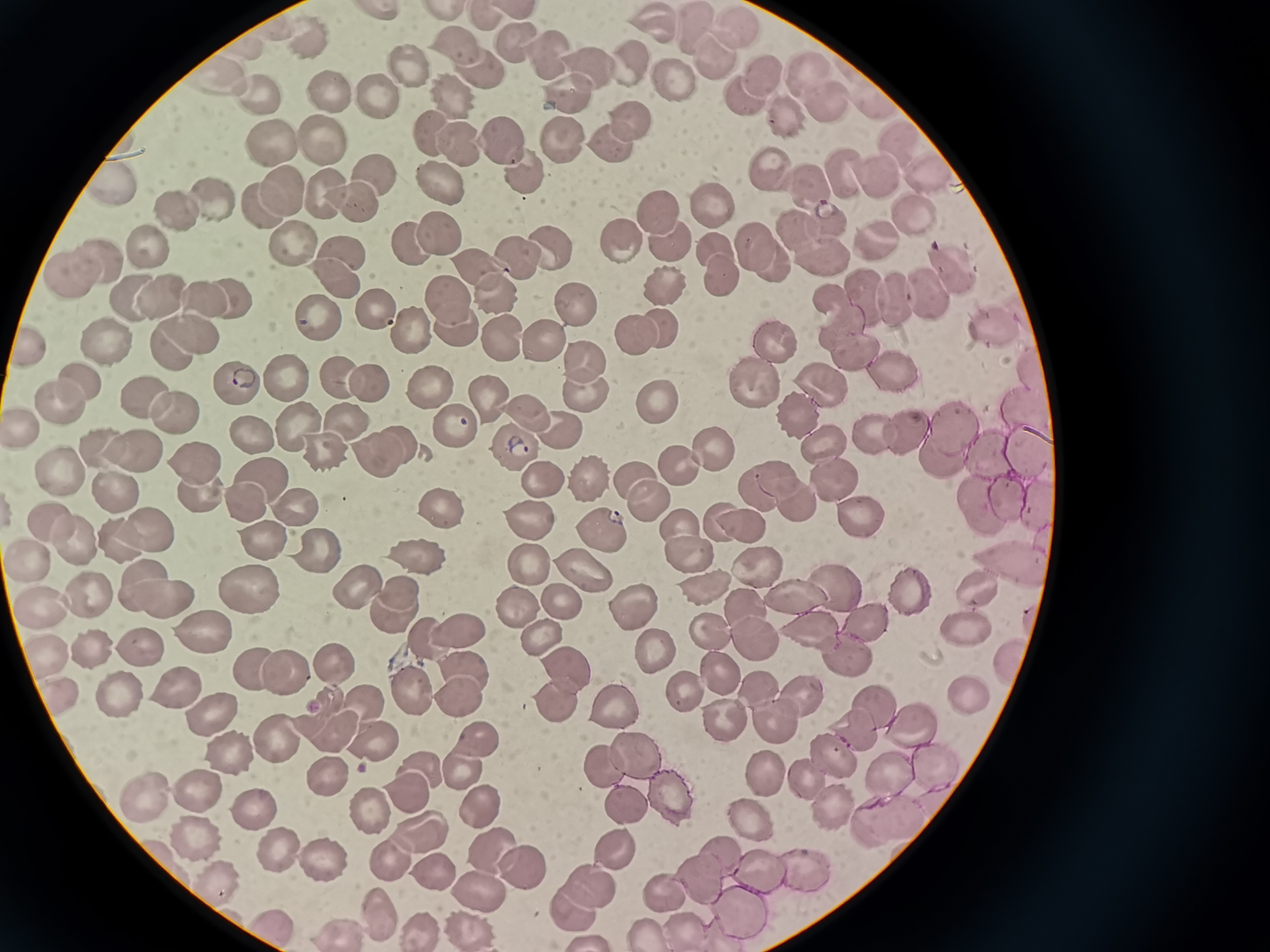

Approximate centers as (x, y) in pixels. Cell locations: (443, 14), (483, 17), (650, 26), (695, 26), (739, 28), (309, 38), (521, 45), (456, 46), (548, 56), (717, 60), (406, 64), (626, 66), (474, 70), (591, 70), (808, 70), (760, 72), (224, 73), (671, 78), (377, 90), (563, 90), (332, 92), (451, 93), (744, 93), (256, 96), (822, 100), (871, 100), (786, 113), (630, 118), (433, 133), (900, 136), (553, 139), (321, 141), (455, 141), (499, 141), (604, 141), (269, 143), (521, 163), (932, 170), (839, 171), (873, 172), (374, 176), (768, 177), (445, 181), (113, 183), (803, 186), (291, 189), (325, 190), (221, 198), (354, 199), (712, 204), (258, 207), (663, 209), (179, 210), (908, 212), (823, 216), (793, 227), (438, 231), (879, 236), (668, 238), (619, 240), (409, 243), (754, 243), (148, 247), (714, 247), (551, 248), (290, 249), (344, 249), (819, 249), (515, 255), (98, 258), (768, 258), (474, 260), (948, 268), (71, 275), (723, 279), (671, 282), (336, 283), (497, 291), (864, 293), (162, 294), (924, 294), (202, 297), (229, 297), (449, 297), (894, 297), (127, 298), (828, 299), (579, 305), (374, 307), (318, 316), (993, 319), (459, 325), (842, 327), (637, 328), (662, 328), (412, 329), (192, 332), (501, 333), (536, 334), (774, 340), (32, 342), (108, 343), (172, 345), (860, 353), (584, 360), (1030, 363), (896, 374), (81, 375), (335, 377), (284, 378), (754, 381), (236, 383), (820, 383), (367, 384), (429, 384), (581, 393), (150, 394), (486, 394), (62, 399), (658, 400), (1025, 406), (525, 409), (170, 413), (797, 415), (298, 417), (347, 418), (453, 423), (26, 425), (558, 425), (951, 426), (907, 428), (879, 433), (245, 437), (397, 439), (510, 440), (826, 440), (1029, 444), (321, 446), (104, 447), (710, 447), (993, 451), (138, 452), (940, 454), (373, 455), (196, 457), (678, 465), (258, 476), (586, 476), (832, 476), (59, 477), (772, 477), (536, 478), (638, 479), (756, 487), (112, 488), (200, 490), (1002, 495), (238, 496), (975, 499), (792, 500), (296, 502), (648, 502), (445, 505), (1039, 505), (856, 514), (713, 517), (529, 518), (47, 520), (739, 522), (599, 531), (677, 534), (145, 535), (119, 537), (259, 541), (73, 547), (325, 549), (684, 549), (418, 556), (527, 559), (35, 560), (1005, 562), (751, 568), (581, 574), (138, 580), (355, 581), (249, 582), (699, 584), (909, 584), (977, 587), (837, 589), (82, 590), (398, 592), (792, 594), (160, 600), (521, 603), (745, 604), (44, 605), (388, 612), (634, 613), (866, 620), (807, 626), (455, 628), (966, 628), (711, 629), (542, 631), (752, 635), (205, 636), (417, 637), (139, 646), (91, 647), (48, 652), (654, 653), (329, 656), (1014, 662), (254, 665), (561, 666), (282, 667), (712, 670), (469, 672), (172, 684), (758, 688), (111, 691), (966, 691), (411, 694), (463, 694), (55, 695), (687, 697), (806, 699), (550, 701), (368, 703), (613, 707), (874, 708), (206, 709), (773, 723), (914, 724), (328, 727), (855, 731), (376, 736), (271, 737), (480, 743), (228, 746), (634, 749), (831, 754), (931, 760), (603, 767), (760, 769), (420, 770), (461, 772), (328, 773), (889, 776), (805, 777), (203, 792), (411, 792), (664, 796), (144, 797), (618, 799), (828, 802), (368, 803), (252, 807), (478, 807), (873, 816), (899, 816), (748, 817), (419, 835), (190, 837), (723, 849), (612, 851), (279, 853), (495, 853), (383, 861), (322, 863), (798, 865), (765, 869), (432, 870), (523, 872), (211, 878), (700, 879), (590, 884), (480, 892), (665, 892), (568, 905), (377, 911), (736, 917), (468, 921), (275, 924), (682, 926), (417, 928), (337, 929), (645, 933). Giemsa-stained preparation. Acquired by smartphone through the microscope eyepiece. Single field of view. Image is 1270×952 pixels. Thin blood film.